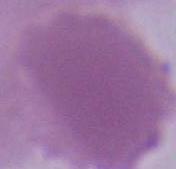
identification = erythrocyte
magnification = 1000x
modality = micrograph